Report the malaria status of this cell.
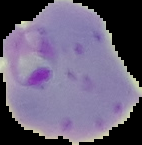
It is parasitized.

image type = segmented cell region with the area outside set to black
image size = 142×145 pixels
preparation = thin blood film